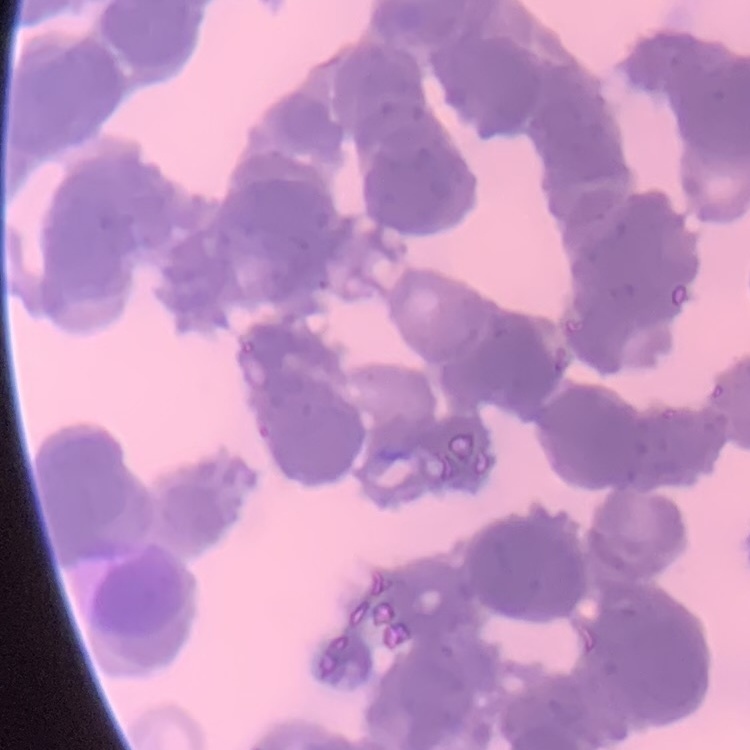 The red blood cells exhibit rouleaux formation. One tile cut from a larger photomicrograph. Field's or Giemsa stain. Thin blood film.